Report the malaria status of this cell.
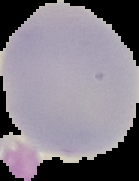

Uninfected.

Summary:
  - Image type: segmented cell region with the area outside set to black
  - Preparation: thin blood film
  - Image size: 139×181 pixels